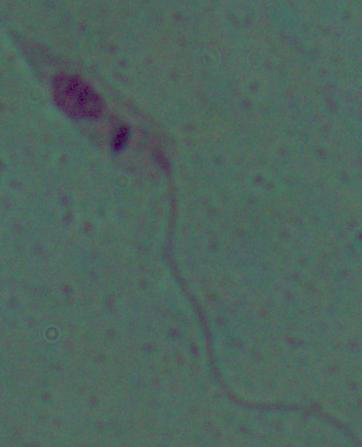

Micrograph. 1000x magnification. A Leishmania parasite is seen.